Identify the parasite.
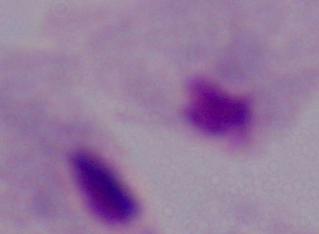
This is a trichomonad.

modality: photomicrograph
magnification: 1000x